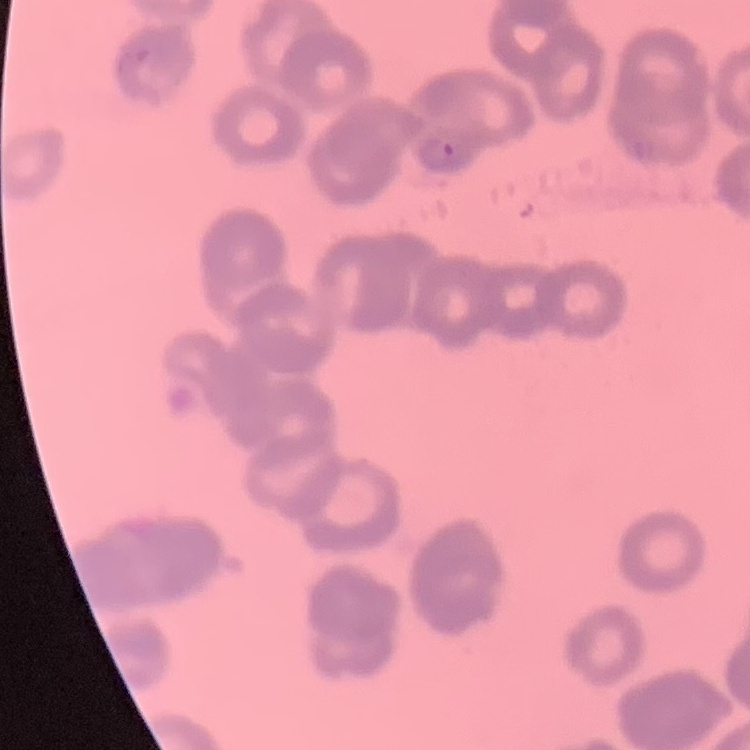

red blood cell morphology = rouleaux formation
stain = Field's or Giemsa
image type = square crop of a larger photomicrograph
preparation = thin blood film